Look for Plasmodium parasites.
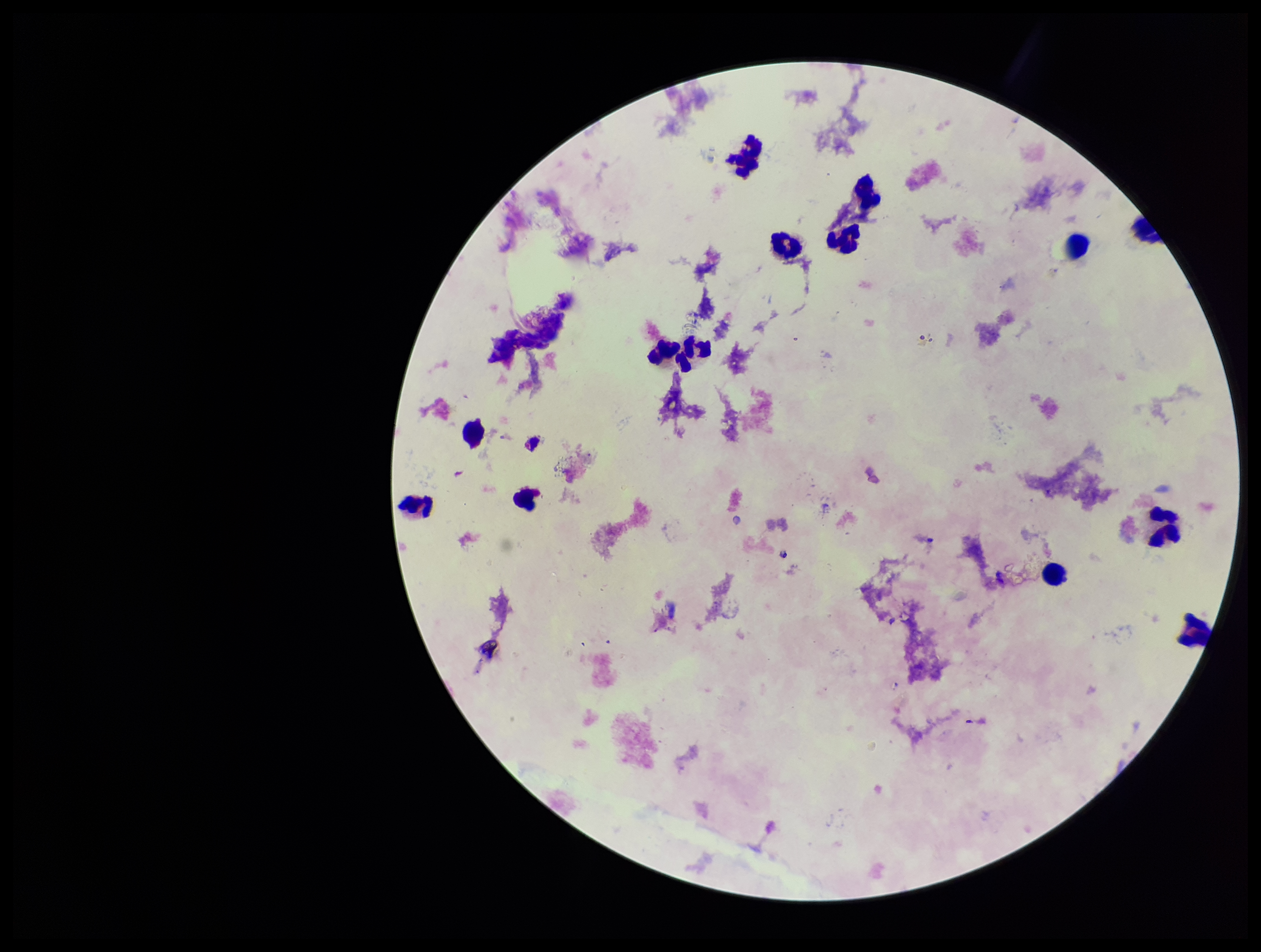

None seen.

Summary:
  - Patient malaria status: negative
  - Capture: smartphone photograph through the microscope eyepiece
  - Stain: Giemsa
  - Preparation: thick smear
  - Field of view: single
  - Image size: 1261×952 pixels
  - Parasite count: 0
  - Leukocyte count: 14